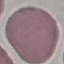
Malaria status: uninfected. Photographed with a smartphone camera at the microscope eyepiece. Giemsa stain. Thin smear of blood. Cell patch, automatically extracted from a larger field of view and resized to 64 × 64 pixels.